Locate and identify every blood parasite.
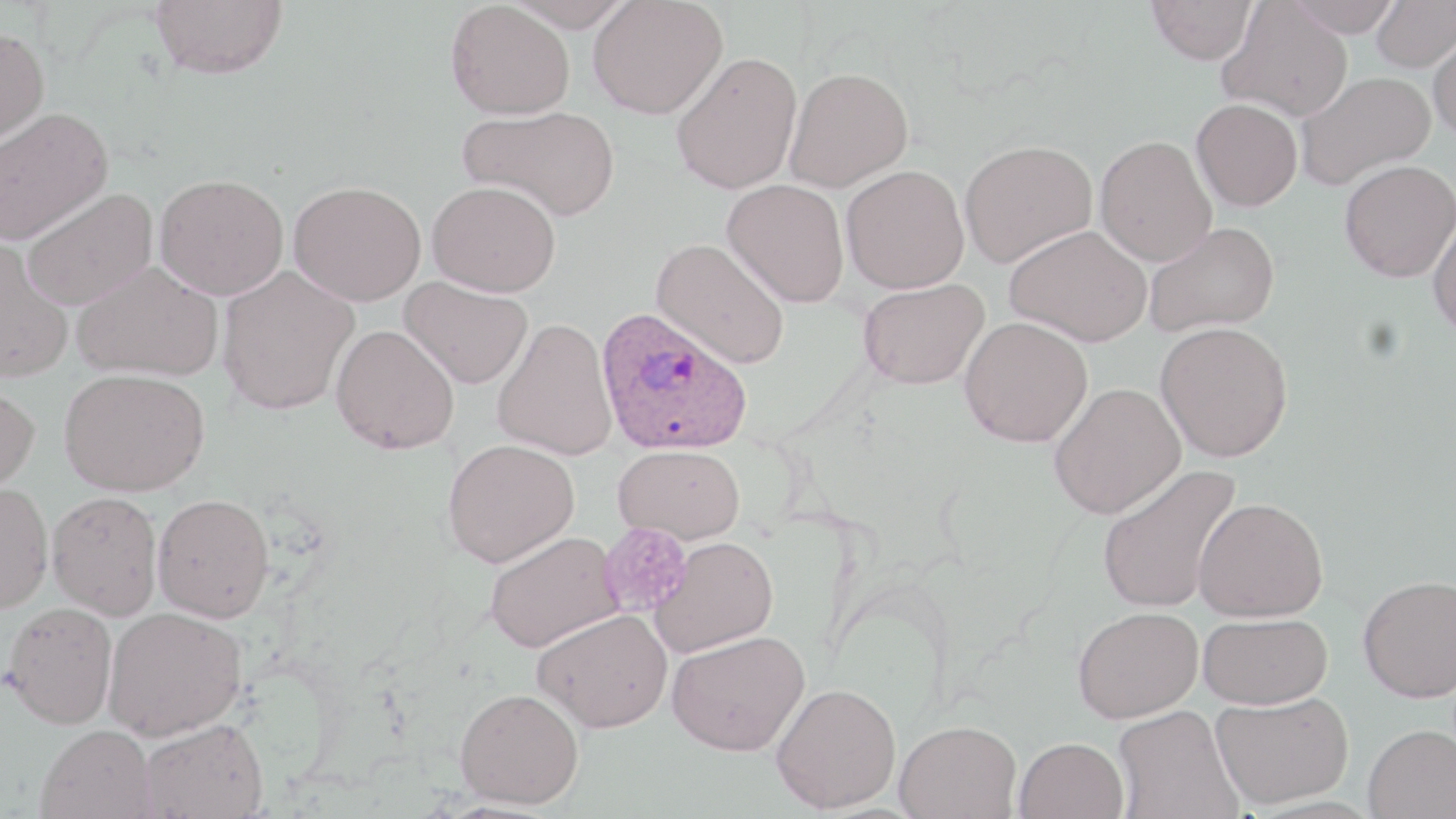

Approximate bounding boxes as [x1, y1, x2, y2] in pixels.
Plasmodium ovale-infected red blood cells: [596, 307, 754, 457].
No Plasmodium falciparum, Plasmodium malariae, Plasmodium vivax, Babesia divergens, or Trypanosoma brucei observed.

slide-level diagnosis = Plasmodium ovale
platelet locations = approximate bounding boxes as [x1, y1, x2, y2] in pixels: [599, 522, 693, 617]
stain = May-Grünwald-Giemsa
magnification = 1000x
modality = light microscopy
image size = 1456×819 pixels
preparation = thin blood film
field of view = single
uninfected red blood cell locations = approximate bounding boxes as [x1, y1, x2, y2] in pixels: [150, 0, 289, 79], [445, 0, 575, 120], [504, 0, 635, 31], [588, 0, 727, 119], [1285, 0, 1404, 37], [1371, 0, 1456, 72], [1147, 1, 1257, 64], [1218, 1, 1353, 121], [0, 26, 50, 149], [1428, 28, 1456, 144], [671, 51, 803, 194], [784, 66, 914, 192], [1294, 71, 1435, 191], [1191, 98, 1303, 211], [458, 104, 621, 221], [0, 107, 113, 245], [1095, 135, 1217, 266], [959, 139, 1097, 268], [1339, 160, 1456, 282], [841, 165, 970, 294], [154, 173, 290, 300], [723, 179, 850, 307], [288, 180, 426, 306], [427, 180, 561, 297], [20, 188, 159, 311], [1429, 208, 1456, 341], [1143, 221, 1280, 337], [1004, 224, 1153, 347], [651, 237, 790, 369], [0, 238, 74, 384], [72, 261, 224, 382], [216, 266, 359, 415], [400, 276, 534, 389], [858, 278, 989, 389], [492, 316, 618, 460], [959, 316, 1093, 447], [1155, 320, 1294, 462], [330, 324, 459, 454], [59, 367, 210, 496], [0, 381, 40, 498], [1048, 383, 1186, 519], [443, 438, 580, 567], [613, 443, 746, 545], [1097, 463, 1243, 614], [0, 482, 53, 614], [47, 491, 163, 620], [152, 493, 275, 623], [1194, 497, 1329, 622], [484, 530, 622, 653], [649, 536, 779, 658], [1358, 574, 1456, 702], [3, 601, 118, 728], [1073, 606, 1203, 723], [103, 607, 247, 740], [532, 608, 673, 732], [1199, 612, 1333, 709], [666, 630, 809, 755], [771, 682, 901, 813], [454, 687, 584, 809], [1211, 691, 1354, 809], [1111, 704, 1244, 819], [139, 718, 268, 818], [895, 720, 1022, 818], [36, 724, 157, 818], [1364, 724, 1455, 819], [1014, 737, 1130, 819]